Comment on the morphology of the erythrocytes.
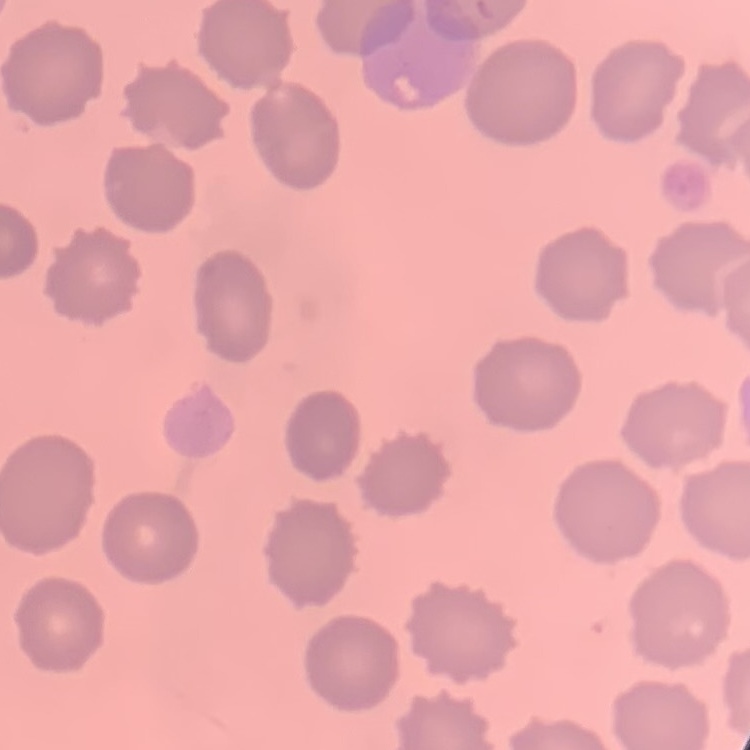
They show no rouleaux formation.

image type = square crop of a larger photomicrograph
stain = Field's or Giemsa
preparation = thin blood film